Comment on the morphology of the erythrocytes.
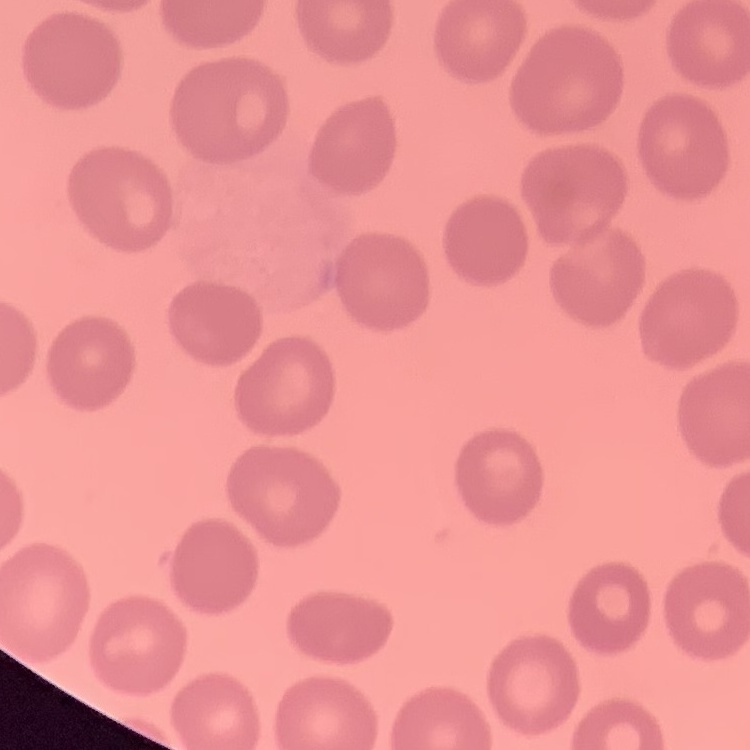
No rouleaux formation.

preparation = thin blood film
stain = Field's or Giemsa
image type = one tile cut from a larger photomicrograph